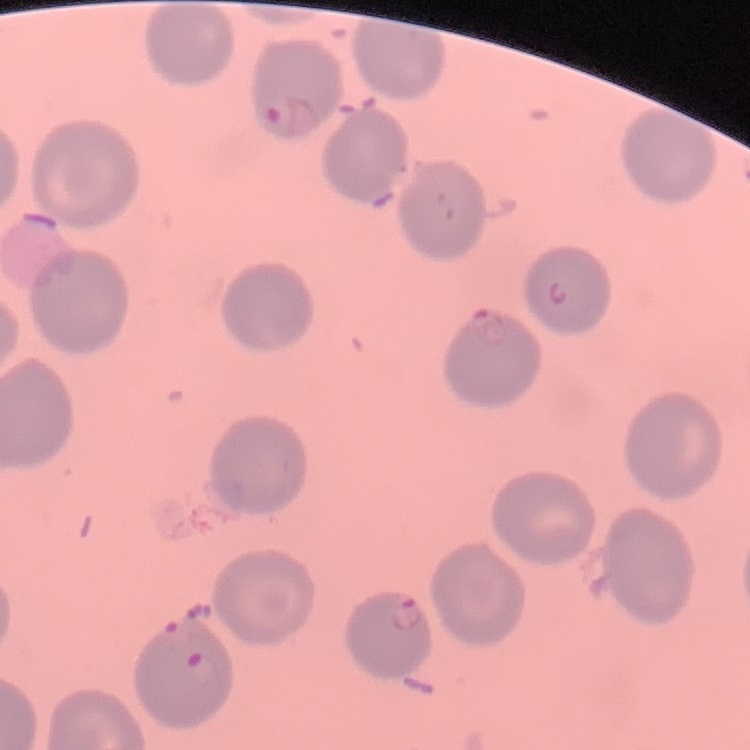
erythrocyte morphology = no rouleaux formation
stain = Field's or Giemsa
preparation = thin blood film
image type = one tile cut from a larger photomicrograph